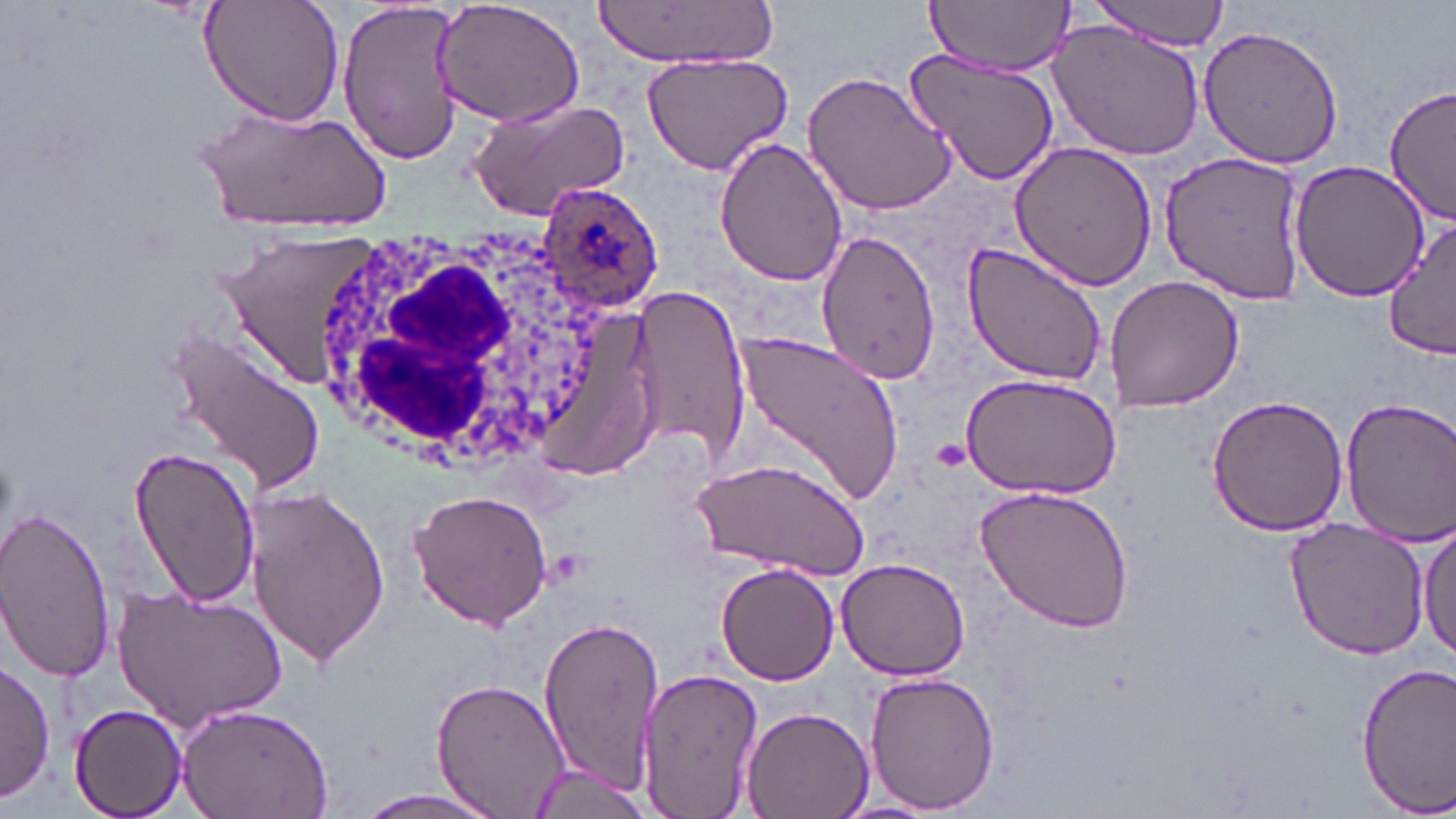

Summary:
  - Coordinate format: approximate bounding boxes as [x1, y1, x2, y2] in pixels
  - Plasmodium ovale-infected red blood cell locations: [540, 180, 663, 315]
  - White blood cell locations: [308, 225, 609, 467]
  - Uninfected red blood cell locations: [200, 0, 344, 126], [337, 0, 464, 167], [591, 0, 777, 68], [920, 0, 1074, 76], [1088, 0, 1230, 47], [432, 1, 587, 129], [1049, 19, 1210, 162], [1197, 23, 1343, 170], [903, 47, 1062, 189], [640, 50, 797, 175], [803, 68, 958, 218], [1385, 83, 1456, 225], [468, 97, 631, 223], [196, 103, 391, 233], [714, 136, 848, 288], [1010, 140, 1160, 291], [1155, 148, 1310, 303], [1288, 159, 1429, 303], [1383, 218, 1456, 362], [211, 226, 392, 390], [813, 226, 941, 384], [961, 240, 1108, 385], [1108, 278, 1244, 412], [631, 283, 751, 469], [164, 323, 326, 499], [732, 326, 902, 512], [954, 373, 1119, 498], [1207, 394, 1350, 538], [1336, 397, 1456, 545], [126, 444, 260, 607], [690, 456, 869, 581], [243, 483, 389, 667], [976, 487, 1134, 632], [408, 489, 554, 631], [0, 504, 119, 687], [1282, 515, 1433, 659], [1417, 521, 1455, 670], [838, 558, 969, 680], [715, 562, 841, 684], [115, 586, 288, 728], [537, 613, 664, 800], [0, 659, 53, 801], [1355, 660, 1456, 811], [635, 667, 763, 819], [863, 671, 1000, 815], [431, 676, 571, 818], [175, 700, 334, 819], [68, 702, 192, 817], [739, 705, 873, 819], [528, 764, 658, 816], [344, 789, 513, 819]
  - Platelet locations: [543, 549, 591, 591]
  - Slide-level diagnosis: Plasmodium ovale
  - Magnification: 1000x
  - Image size: 1456×819 pixels
  - Field of view: one of a larger specimen
  - Stain: May-Grünwald-Giemsa
  - Preparation: thin blood film
  - Modality: light microscopy